Classify this cell by malaria status.
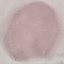
Uninfected.

Giemsa-stained preparation. Thin blood smear. Photographed with a smartphone camera at the microscope eyepiece. Automatically extracted cell patch, resized to 64 × 64 pixels.